Assess for malaria.
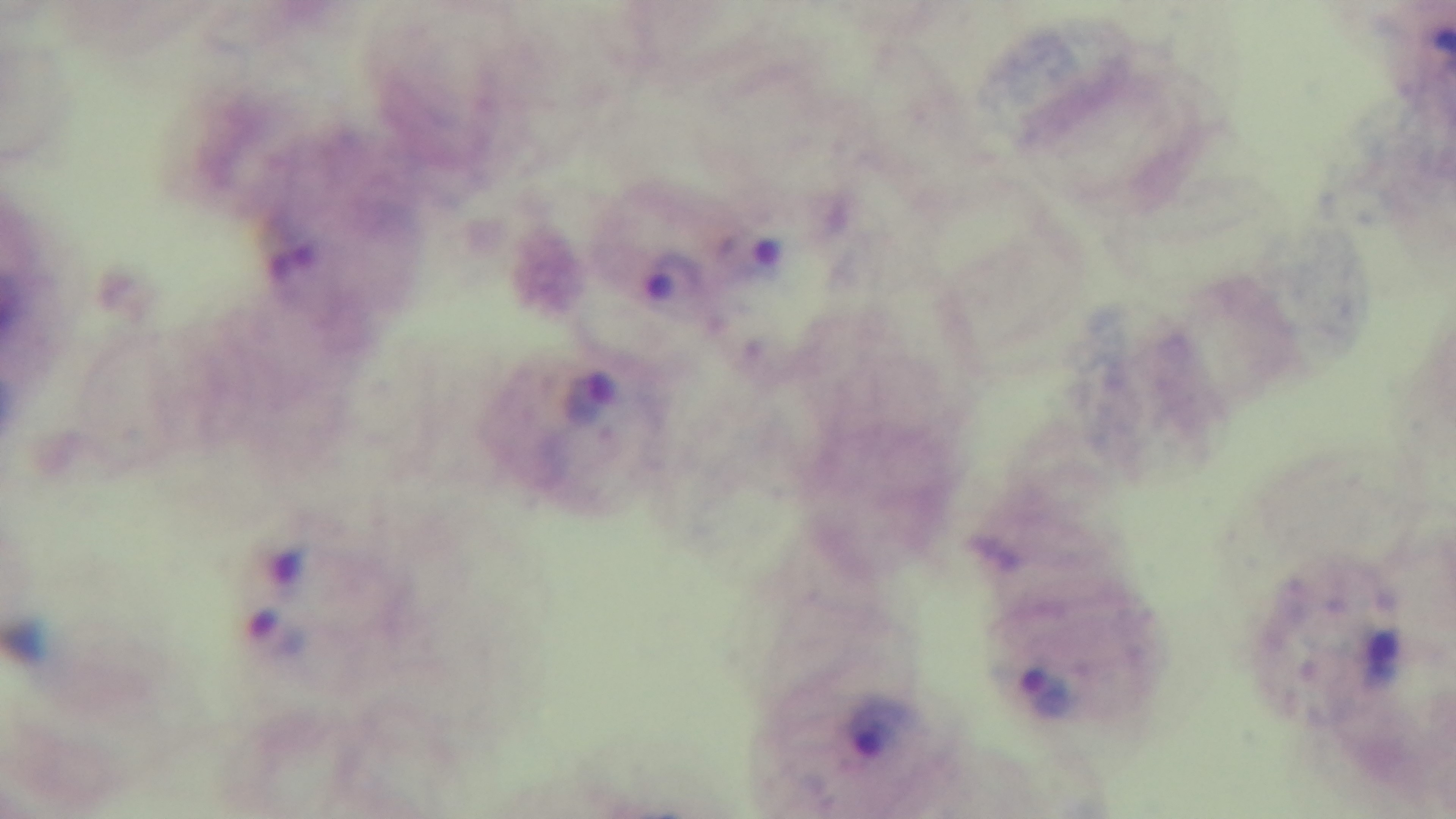

It is infected.

Summary:
  - Stain: Giemsa
  - Preparation: thick blood film
  - Field of view: single
  - Objective: 100x oil immersion
  - Modality: light microscopy
  - Capture: mounted 4K digital camera